Identify the parasite.
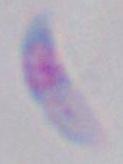

Toxoplasma gondii.

Summary:
  - Magnification: 1000x
  - Modality: micrograph